Report the malaria status of this cell.
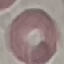
Uninfected.

capture: smartphone camera at the microscope eyepiece
image_type: automatically extracted cell patch, resized to 64 × 64 pixels
stain: Giemsa
preparation: thin blood smear